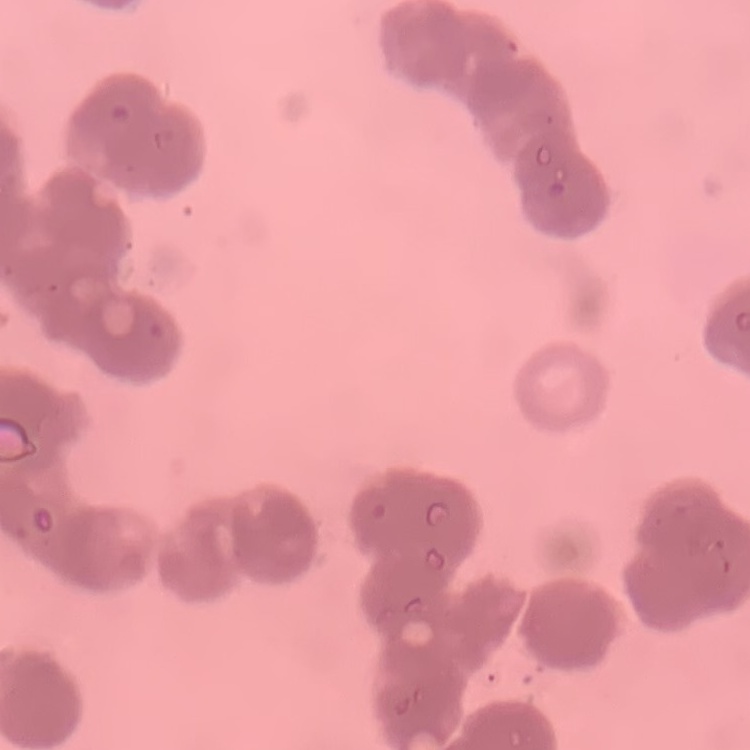
erythrocyte morphology = rouleaux formation
stain = Field's or Giemsa
image type = square crop of a larger photomicrograph
preparation = thin blood film